Name the parasite shown.
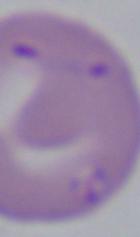

Babesia.

1000x magnification. Micrograph.